Comment on the morphology of the erythrocytes.
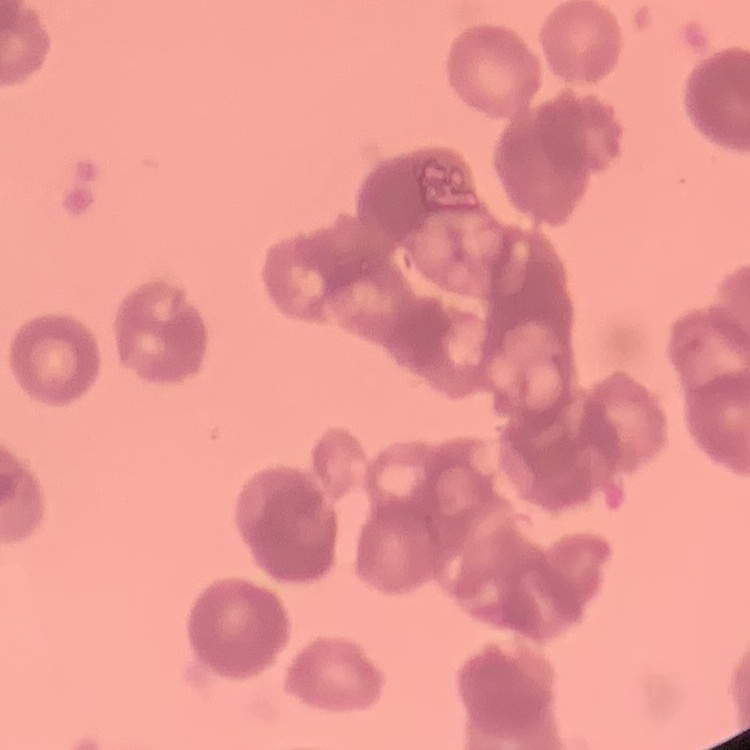
They show rouleaux formation.

image type = one tile cut from a larger photomicrograph
stain = Field's or Giemsa
preparation = thin peripheral smear